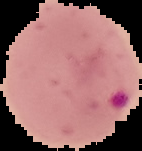

Summary:
  - Malaria status: parasitized
  - Image type: segmented cell region on a black background
  - Preparation: thin blood film
  - Image size: 142×151 pixels